Mark where platelets are.
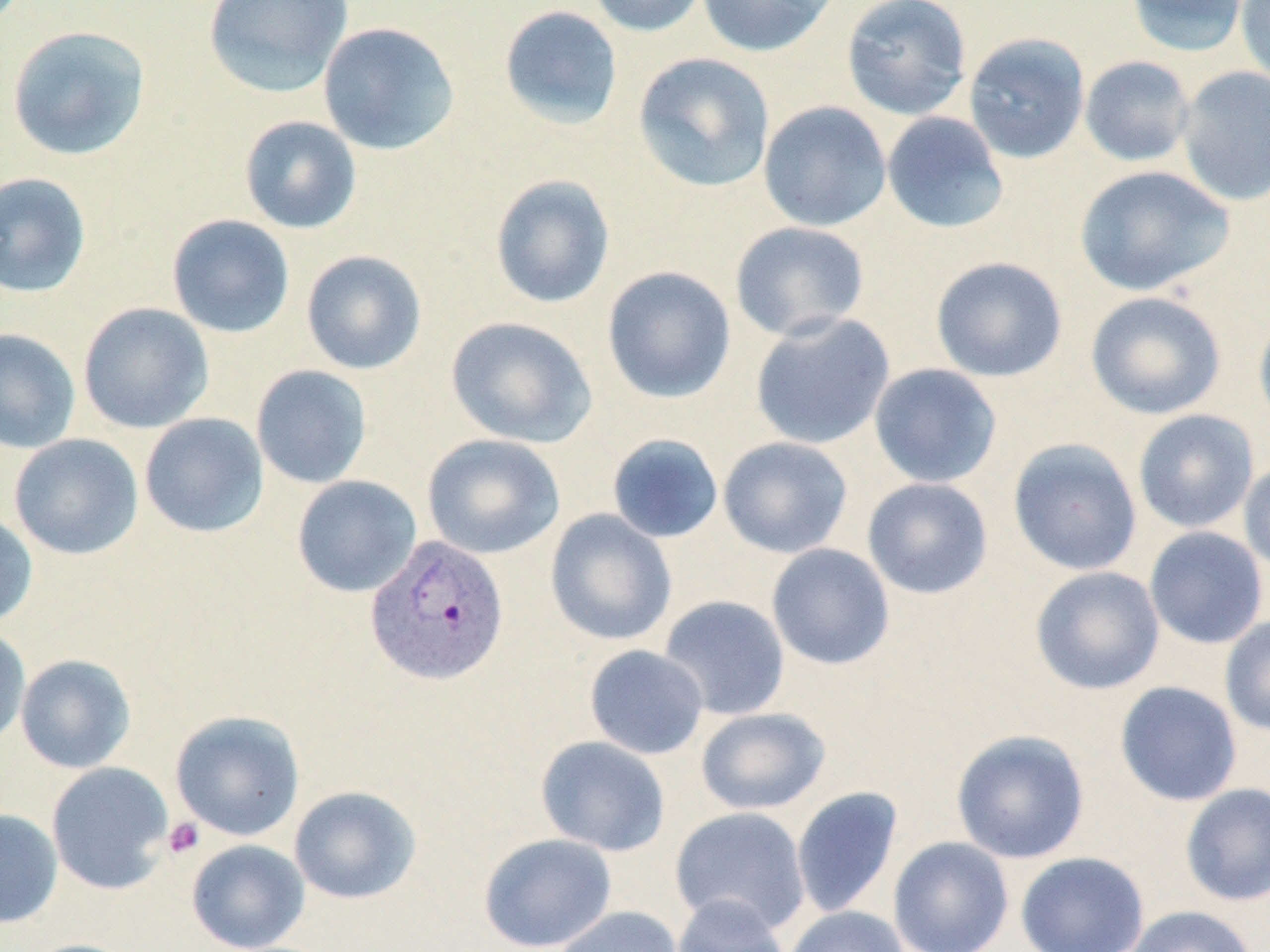
Approximate bounding boxes as [x1, y1, x2, y2] in pixels.
Platelets: [163, 818, 204, 858].

slide-level diagnosis = Plasmodium vivax
image size = 1270×952 pixels
uninfected red blood cell locations = approximate bounding boxes as [x1, y1, x2, y2] in pixels: [203, 0, 353, 98], [585, 0, 709, 37], [696, 0, 838, 57], [841, 0, 973, 121], [1125, 0, 1250, 57], [1235, 0, 1270, 88], [498, 5, 624, 130], [318, 21, 460, 156], [6, 24, 151, 161], [963, 32, 1090, 164], [632, 52, 775, 193], [1079, 55, 1196, 167], [1176, 66, 1270, 206], [758, 101, 892, 232], [881, 111, 1009, 235], [238, 115, 362, 234], [1073, 165, 1235, 297], [0, 172, 92, 298], [489, 174, 616, 309], [166, 214, 295, 339], [729, 221, 869, 342], [301, 249, 427, 375], [930, 256, 1068, 383], [601, 266, 737, 404], [1085, 291, 1226, 419], [77, 302, 214, 434], [1253, 309, 1270, 433], [749, 313, 895, 451], [445, 316, 597, 449], [0, 328, 81, 454], [868, 363, 1002, 488], [251, 365, 372, 489], [1132, 409, 1259, 534], [139, 413, 269, 538], [8, 433, 143, 560], [422, 433, 566, 560], [606, 433, 724, 544], [717, 437, 853, 558], [1008, 438, 1142, 576], [1239, 457, 1270, 577], [291, 475, 422, 598], [862, 477, 993, 600], [544, 509, 677, 647], [0, 512, 38, 629], [1144, 526, 1269, 649], [766, 543, 896, 670], [1030, 566, 1165, 695], [658, 595, 791, 720], [1220, 615, 1270, 737], [0, 626, 31, 748], [584, 645, 709, 760], [15, 654, 136, 774], [1114, 681, 1243, 807], [695, 707, 831, 815], [169, 709, 305, 842], [951, 730, 1089, 864], [535, 735, 671, 856], [46, 762, 174, 895], [1180, 783, 1270, 906], [288, 786, 421, 904], [791, 786, 904, 919], [669, 806, 811, 937], [0, 809, 63, 928], [478, 833, 617, 952], [888, 837, 1014, 952], [186, 839, 310, 951], [1015, 852, 1150, 952], [671, 894, 791, 952], [551, 905, 683, 952], [1125, 905, 1257, 952], [783, 906, 909, 952], [18, 938, 142, 952]
modality = optical microscopy
preparation = thin blood film
Plasmodium vivax-infected red blood cell locations = approximate bounding boxes as [x1, y1, x2, y2] in pixels: [365, 534, 509, 685]
stain = May-Grünwald-Giemsa
magnification = 1000x
field of view = single